Give the position of every Plasmodium parasite visible.
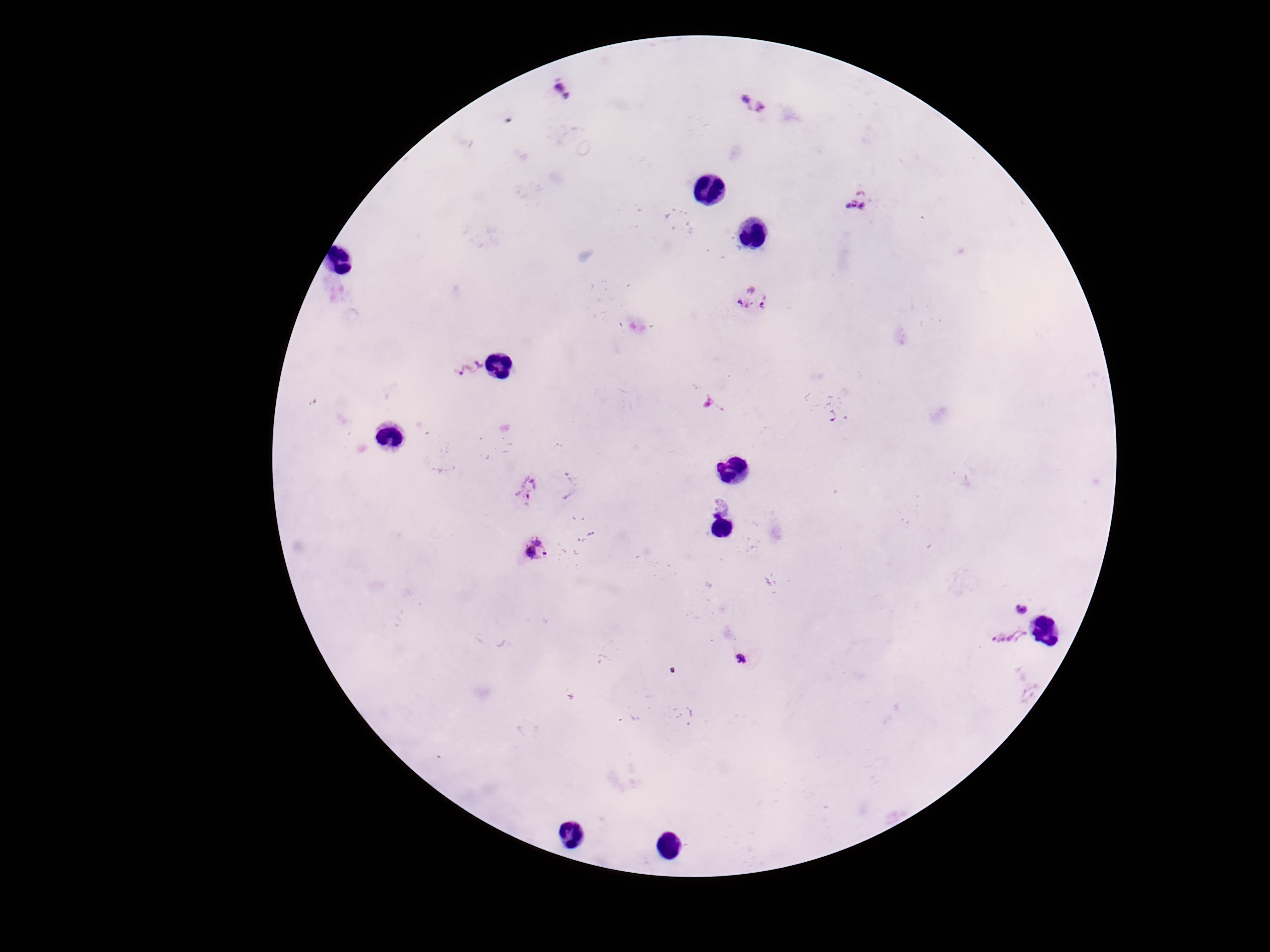
Approximate centers as {x, y} in pixels.
Plasmodium parasites: {562, 89}, {753, 106}, {860, 203}, {750, 301}, {469, 370}, {714, 406}, {528, 489}, {720, 505}, {534, 550}, {1021, 605}, {1007, 642}, {740, 659}.

Summary:
  - Patient malaria status: positive
  - Stain: Giemsa
  - Preparation: thick peripheral-blood smear
  - Capture: smartphone camera through the microscope eyepiece
  - Image size: 1270×952 pixels
  - Field of view: single
  - Magnification: 100x